Point out each Plasmodium parasite.
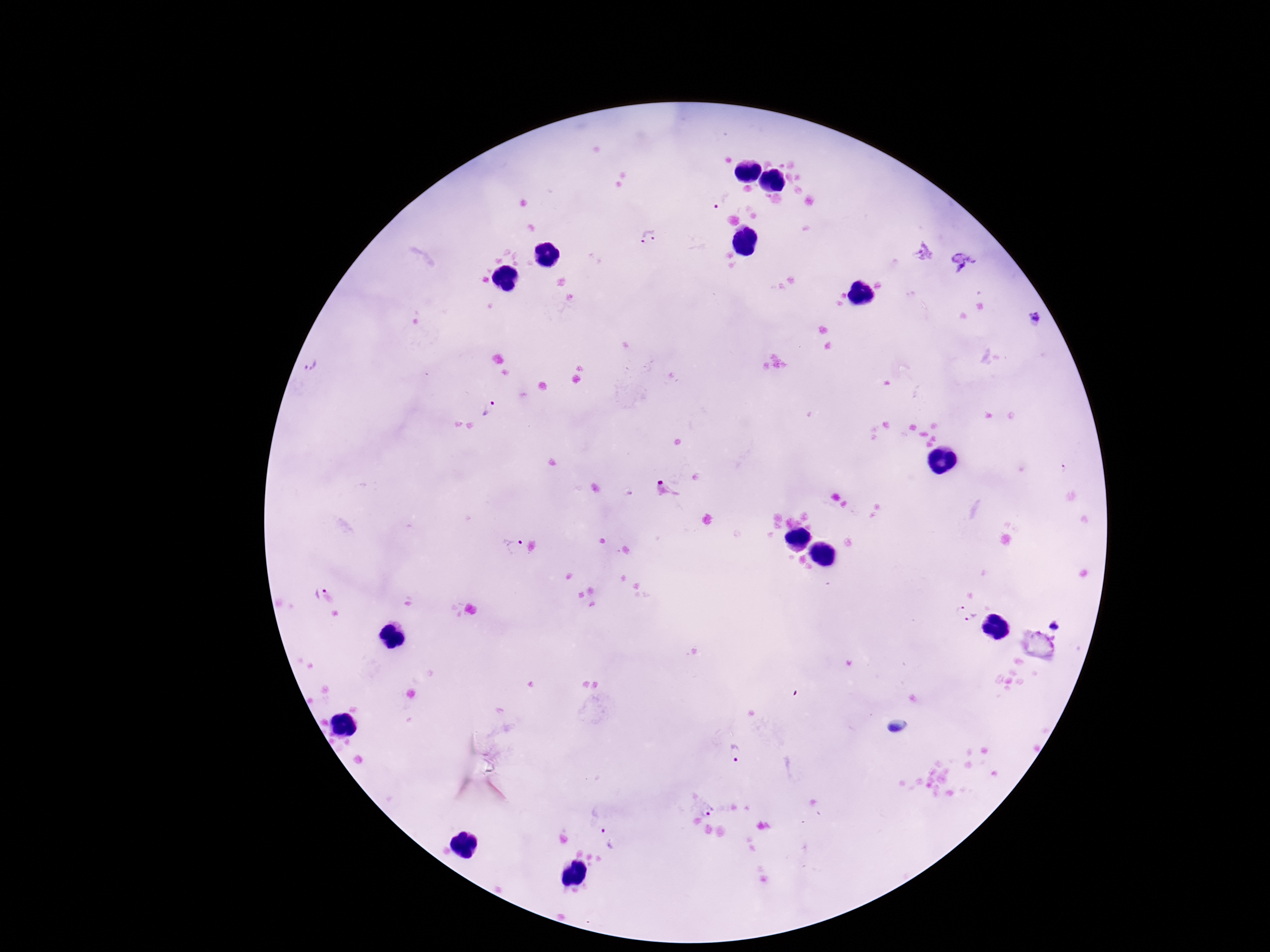
Approximate object centers, in pixels from the top-left corner.
Plasmodium parasites: (x=723, y=199), (x=650, y=238), (x=1036, y=320), (x=310, y=366), (x=494, y=408), (x=666, y=490), (x=508, y=545), (x=312, y=592), (x=960, y=609), (x=975, y=618), (x=1055, y=626), (x=735, y=752), (x=707, y=811), (x=608, y=839).

Patient malaria status: positive. 100x magnification. Photographed through the microscope eyepiece with a smartphone camera. Giemsa stain. Thick peripheral-blood smear. One field from this slide. Image is 1270×952 pixels.